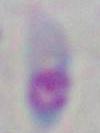
Captured at 1000x magnification. Micrograph. Toxoplasma gondii is shown.